Report the malaria status of this cell.
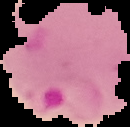

Parasitized.

From a thin blood smear. Segmented cell region on a black background. Image is 130×127 pixels.